State which parasite is depicted.
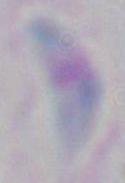

This is Toxoplasma gondii.

Summary:
  - Modality: micrograph
  - Magnification: 1000x